Identify the parasite.
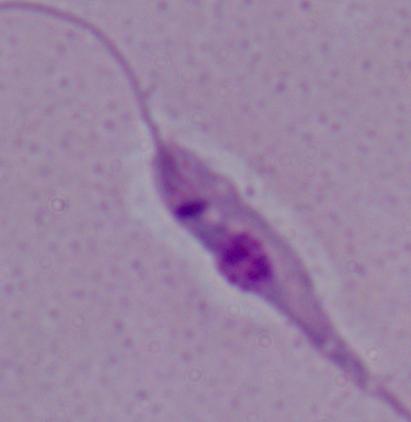

Leishmania.

Micrograph. 1000x magnification.